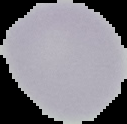

{
  "preparation": "thin blood film",
  "image_type": "segmented cell region with the area outside set to black",
  "image_size": "127×124 pixels",
  "result": "no malaria parasites detected"
}